Comment on the morphology of the erythrocytes.
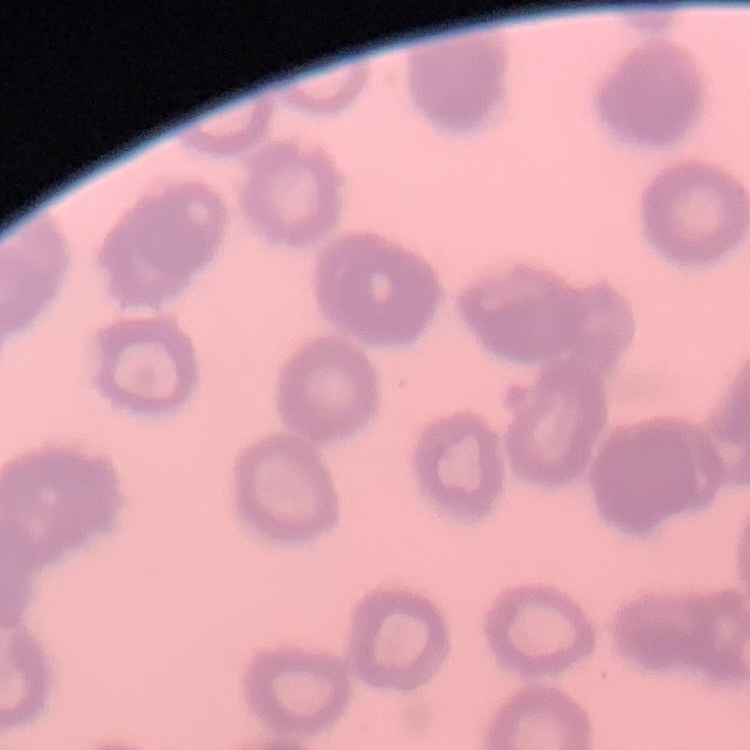

Rouleaux formation.

stain = Field's or Giemsa
preparation = thin peripheral smear
image type = one tile cut from a larger photomicrograph